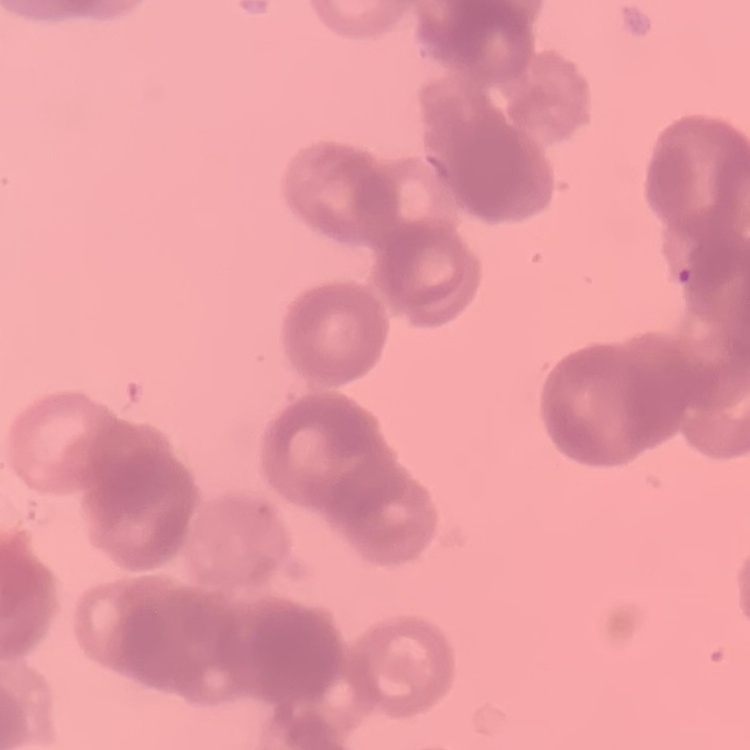
Summary:
  - Erythrocyte morphology: rouleaux formation
  - Image type: one tile cut from a larger photomicrograph
  - Stain: Field's or Giemsa
  - Preparation: thin blood smear